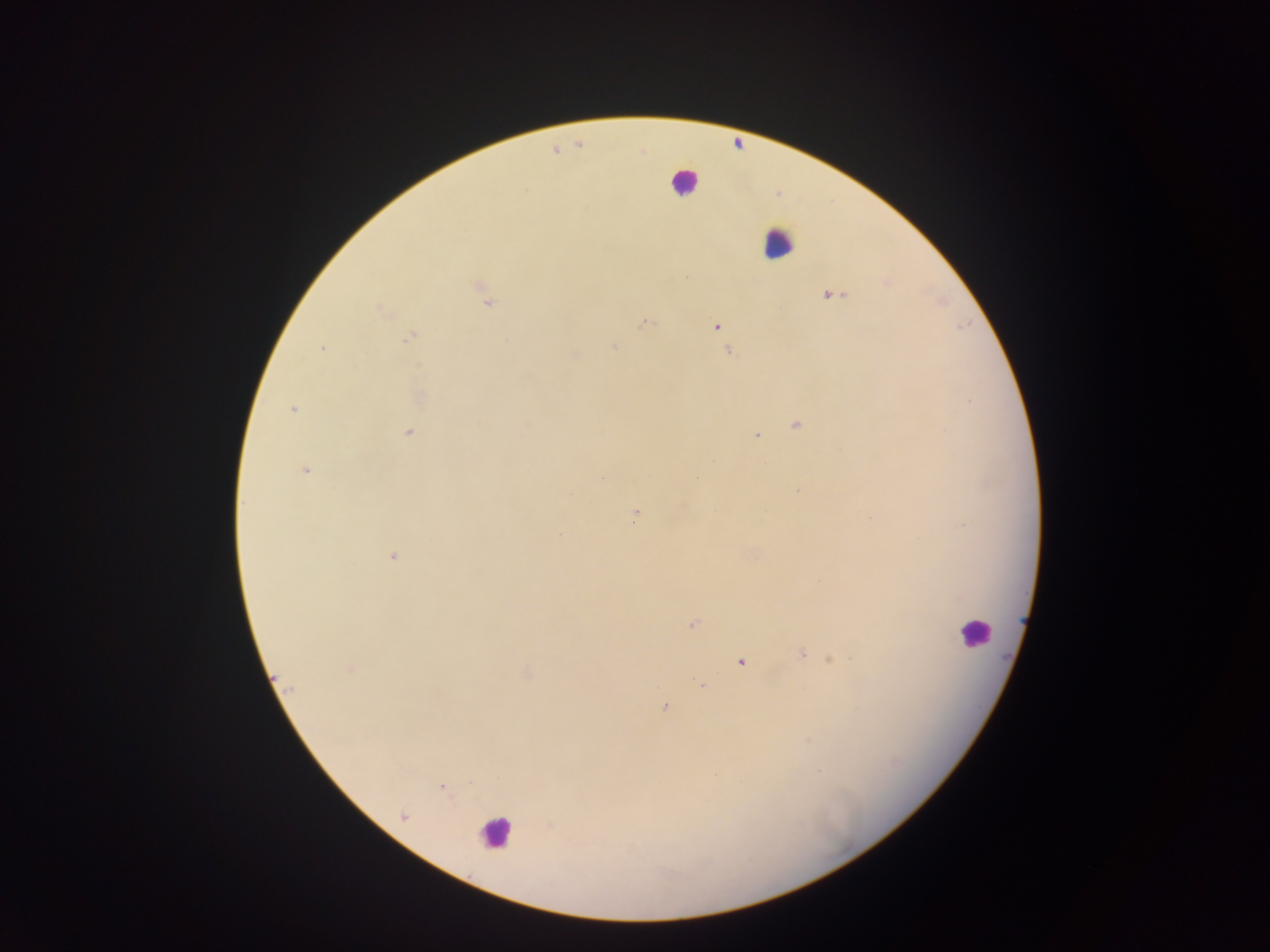
Approximate centers as [x, y] in pixels.
Summary:
  - Leukocyte locations: [683, 182], [777, 244], [973, 631], [494, 833]
  - Plasmodium parasite locations: [832, 296], [487, 303], [380, 309], [646, 323], [716, 326], [410, 338], [723, 342], [614, 347], [322, 349], [729, 351], [574, 355], [292, 409], [796, 425], [408, 433], [757, 436], [713, 460], [304, 470], [797, 491], [635, 515], [392, 557], [693, 625], [802, 653], [834, 659], [741, 662], [351, 669], [702, 684], [289, 687], [664, 707], [441, 787]
  - Image size: 1270×952 pixels
  - Preparation: thick blood film
  - Capture: mobile-phone photograph through a microscope
  - Country: Ghana
  - Field of view: single